Report the malaria status of this cell.
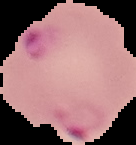
Parasitized.

image_type: cell region segmented out of the field of view; surrounding area masked to black
image_size: 136×145 pixels
preparation: thin blood film